Locate every Plasmodium parasite.
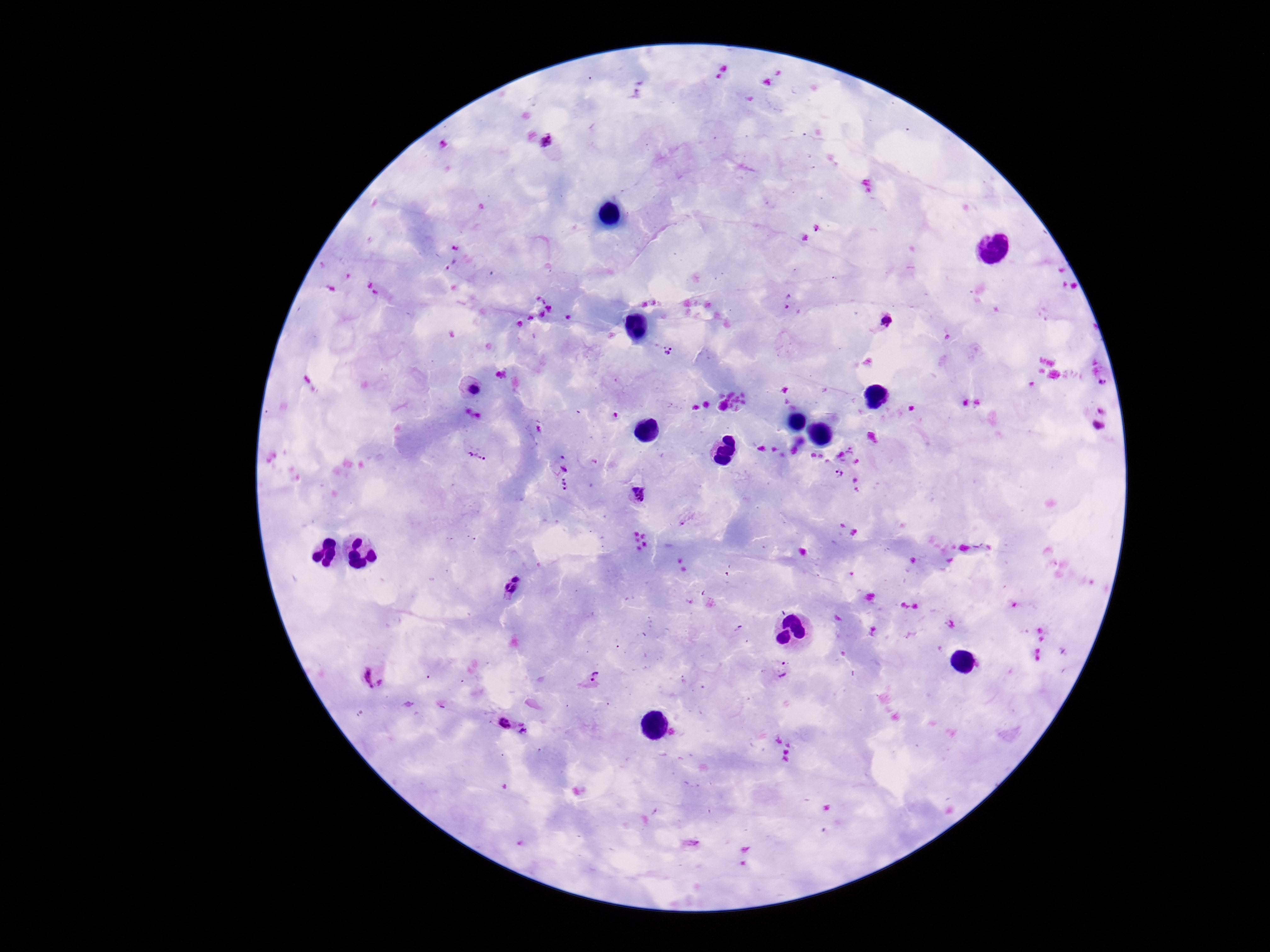
Approximate object centers, in pixels from the top-left corner.
Plasmodium parasites: (x=724, y=67), (x=718, y=76), (x=545, y=142), (x=816, y=228), (x=806, y=238), (x=542, y=299), (x=787, y=302), (x=550, y=309), (x=541, y=314), (x=529, y=317), (x=887, y=323), (x=519, y=325), (x=670, y=352), (x=1103, y=383), (x=472, y=385), (x=732, y=402), (x=710, y=404), (x=695, y=408), (x=1104, y=410), (x=466, y=411), (x=615, y=415), (x=479, y=416), (x=1099, y=426), (x=476, y=453), (x=563, y=458), (x=564, y=469), (x=840, y=472), (x=565, y=485), (x=636, y=494), (x=517, y=577), (x=510, y=589), (x=781, y=669), (x=374, y=676), (x=592, y=677), (x=505, y=723), (x=525, y=729).

Image is 1270×952 pixels. Thick blood smear. 100x magnification. Giemsa stain. Patient malaria status: infected. Photographed through the microscope eyepiece with a smartphone camera. One field from this slide.